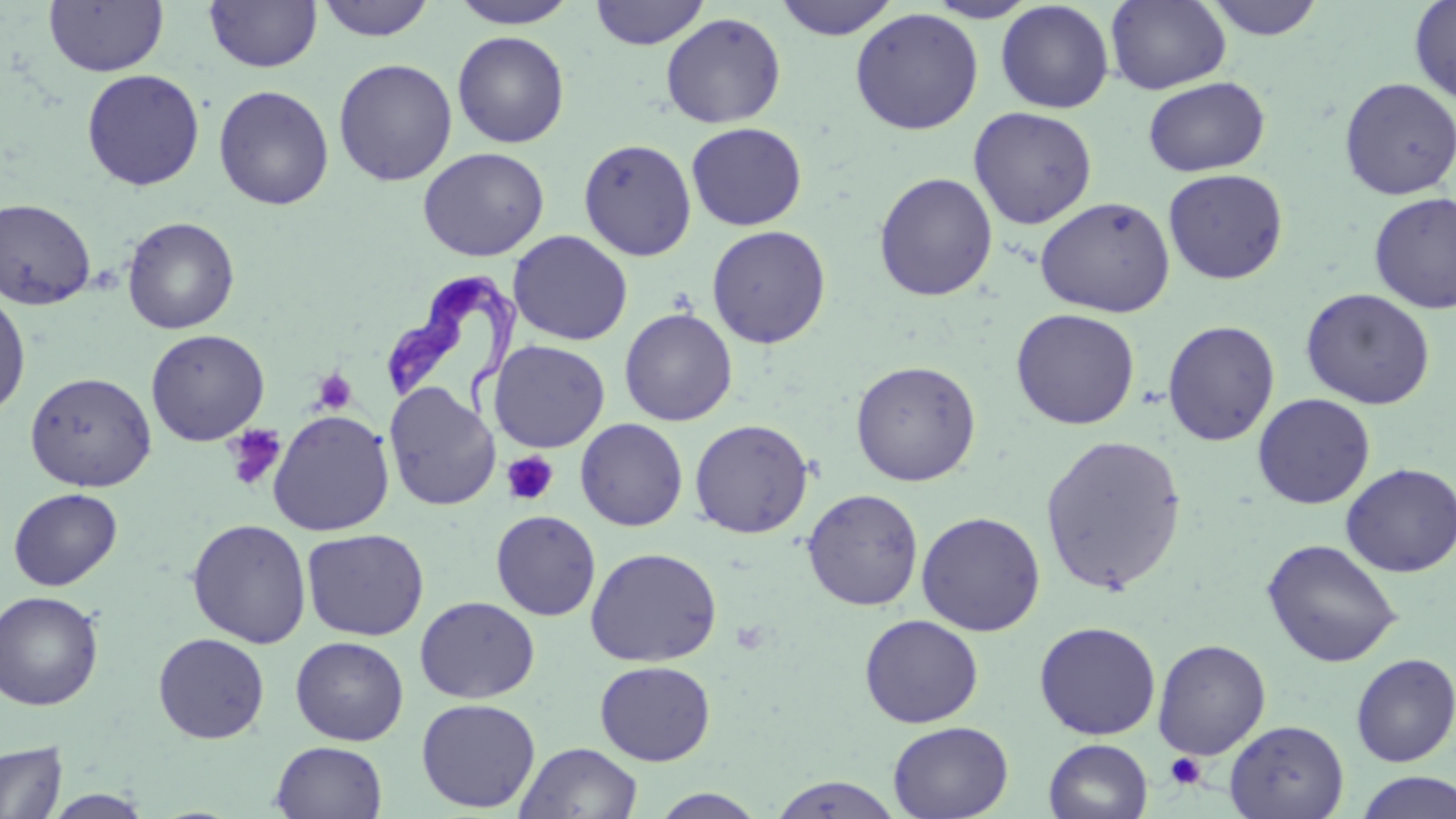

slide_level_diagnosis: Trypanosoma brucei
modality: optical microscopy
image_size: 1456×819 pixels
magnification: 1000x
preparation: thin blood smear
uninfected_red_blood_cell_locations: 'approximate bounding boxes as (x1,y1)-(x2,y2) corner pairs in pixels: (43,0)-(168,77), (204,0)-(323,73), (315,0)-(436,42), (448,0)-(580,28), (773,0)-(900,40), (1105,0)-(1231,94), (1204,0)-(1325,41), (1408,0)-(1456,105), (589,1)-(710,49), (924,1)-(1039,22), (995,2)-(1114,114), (849,8)-(984,135), (660,12)-(786,129), (452,30)-(570,148), (333,58)-(457,186), (81,68)-(205,191), (214,76)-(459,197), (1142,76)-(1270,177), (1338,77)-(1455,200), (213,84)-(335,210), (968,106)-(1098,229), (685,122)-(807,231), (578,138)-(697,261), (418,146)-(549,261), (1162,168)-(1288,285), (873,172)-(998,301), (1368,191)-(1456,314), (1034,196)-(1175,318), (0,198)-(96,310), (122,216)-(240,334), (706,225)-(832,348), (507,230)-(633,346), (1300,288)-(1435,409), (0,289)-(31,418), (619,307)-(738,426), (1010,308)-(1140,430), (1162,319)-(1280,446), (145,329)-(270,446), (489,339)-(610,452), (850,359)-(981,487), (25,371)-(157,492), (383,383)-(500,511), (1252,393)-(1375,509), (268,409)-(395,536), (575,418)-(688,531), (689,418)-(813,538), (1040,434)-(1187,595), (1341,462)-(1456,577), (8,487)-(122,591), (802,488)-(924,611), (490,509)-(601,620), (916,511)-(1045,636), (186,517)-(313,648), (301,527)-(429,641), (1261,538)-(1403,668), (585,546)-(723,667), (0,590)-(104,711), (414,595)-(540,704), (860,614)-(984,728), (1034,621)-(1161,740), (152,632)-(270,744), (291,636)-(409,745), (1153,638)-(1271,760), (1351,653)-(1456,766), (594,660)-(715,766), (416,698)-(541,813), (1224,719)-(1349,819), (887,721)-(1013,818), (1043,738)-(1153,819), (0,740)-(68,819), (270,741)-(388,819), (514,741)-(644,819), (1354,771)-(1456,819), (766,775)-(906,818), (648,788)-(769,818), (44,789)-(154,818)'
field_of_view: one of a larger specimen
platelet_locations: 'approximate bounding boxes as (x1,y1)-(x2,y2) corner pairs in pixels: (311,369)-(357,415), (224,425)-(286,491), (502,452)-(558,506), (1165,752)-(1207,790)'
trypanosoma_brucei_locations: 'approximate bounding boxes as (x1,y1)-(x2,y2) corner pairs in pixels: (387,272)-(527,419)'
stain: May-Grünwald-Giemsa